Classify this cell by malaria status.
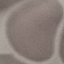

It is uninfected.

Automatically extracted cell patch, resized to 64 × 64 pixels. Giemsa stain. Acquired by smartphone through the microscope eyepiece. Thin blood smear.